Point out each Plasmodium parasite.
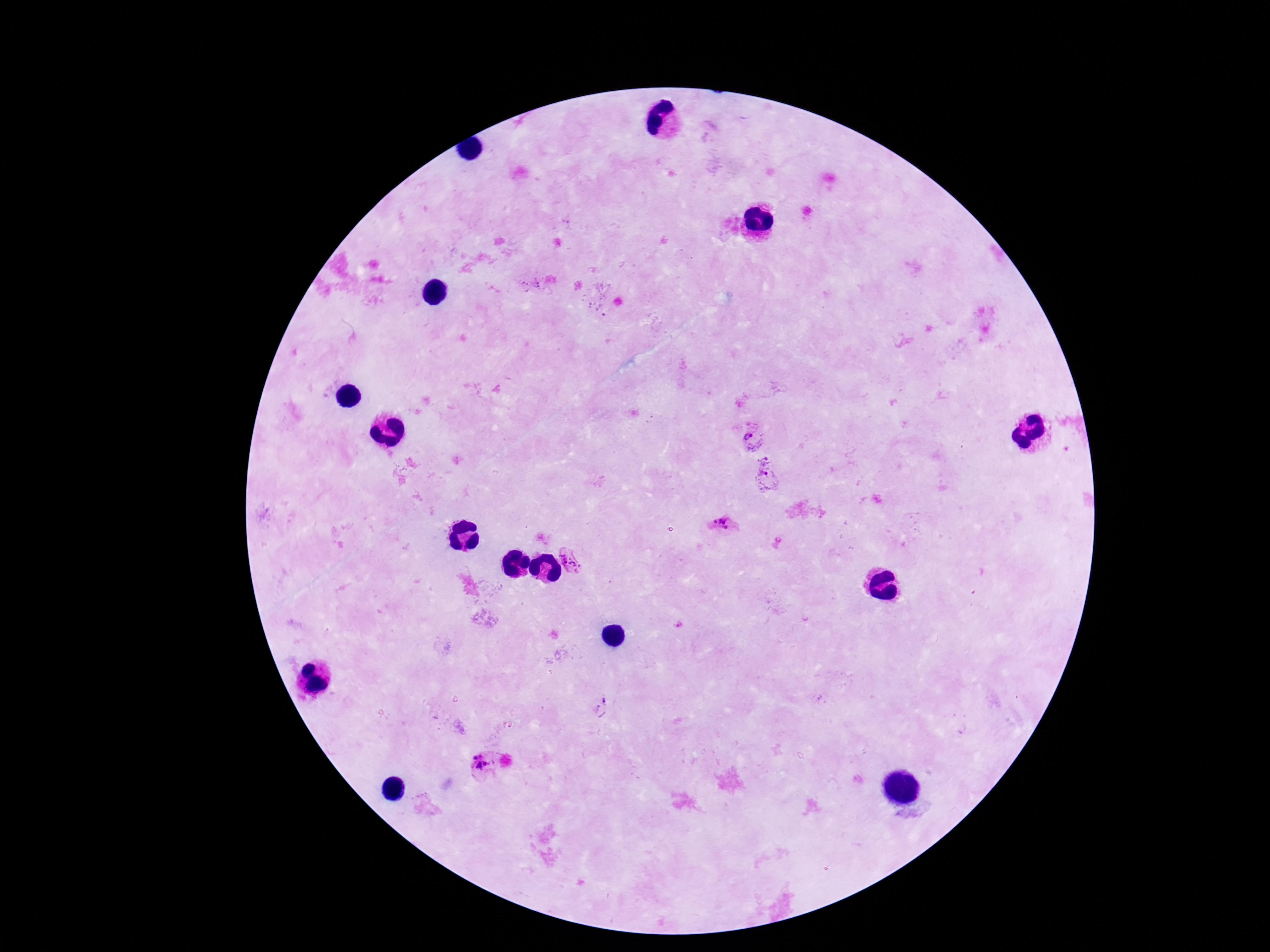

Approximate centers as [x, y] in pixels.
Plasmodium parasites: [753, 435], [766, 468], [723, 524], [572, 561], [602, 706], [482, 764].

{
  "field_of_view": "one from this slide",
  "stain": "Giemsa",
  "patient_malaria_status": "positive",
  "image_size": "1270×952 pixels",
  "magnification": "100x",
  "capture": "smartphone camera through the microscope eyepiece",
  "preparation": "thick blood film"
}